Locate and identify every blood parasite.
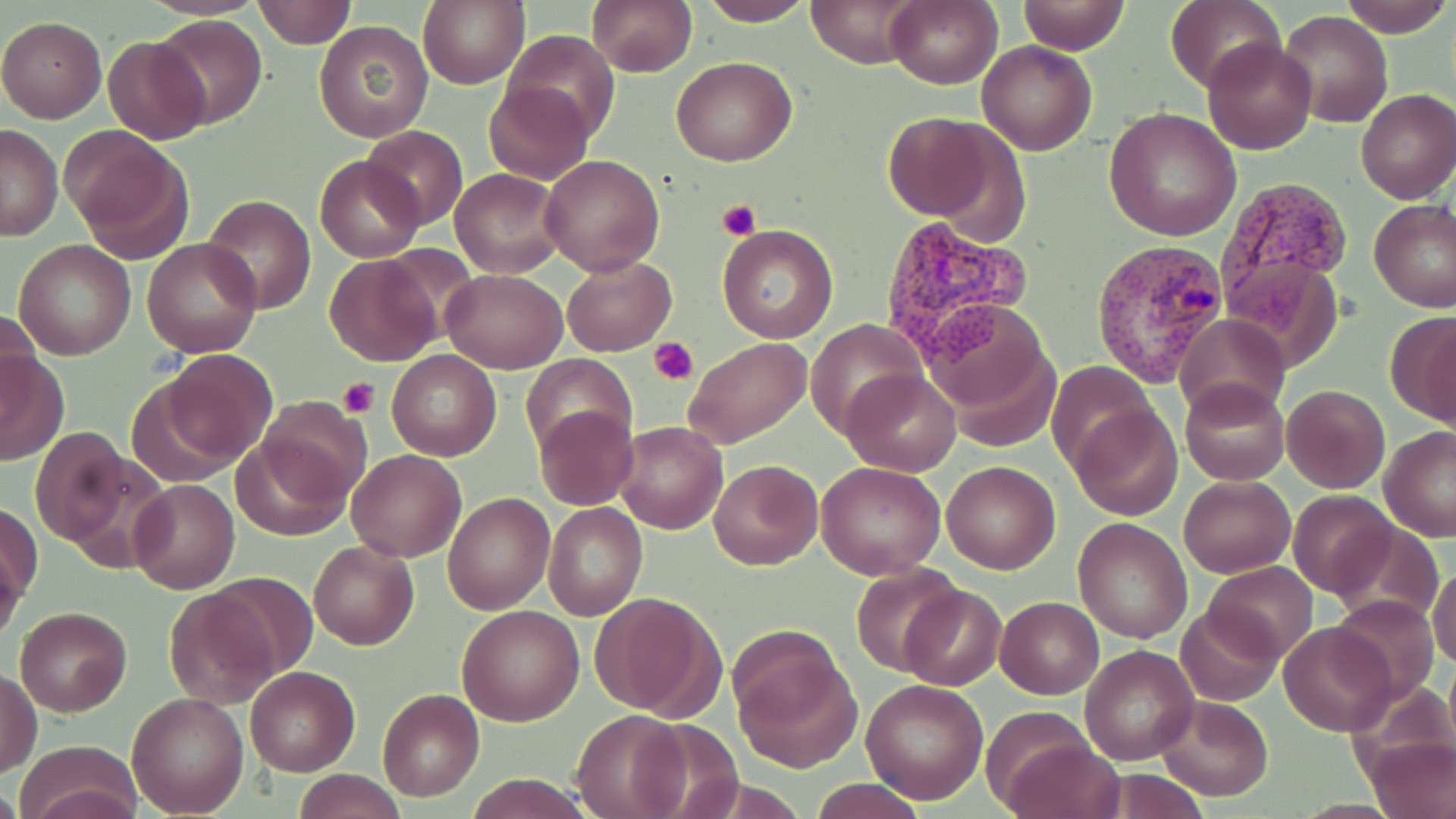

Approximate bounding boxes as (x1,y1)-(x2,y2) corner pairs in pixels.
Plasmodium vivax-infected red blood cells: (1218,177)-(1351,303), (875,213)-(1032,361), (1089,239)-(1229,387).
No Plasmodium falciparum, Plasmodium ovale, Plasmodium malariae, Babesia divergens, or Trypanosoma brucei observed.

slide_level_diagnosis: Plasmodium vivax
field_of_view: one of a larger specimen
platelet_locations: 'approximate bounding boxes as (x1,y1)-(x2,y2) corner pairs in pixels: (718,199)-(760,240), (649,338)-(697,384), (339,376)-(380,417)'
stain: May-Grünwald-Giemsa
magnification: 1000x
image_size: 1456×819 pixels
modality: optical microscopy
preparation: thin blood smear
uninfected_red_blood_cell_locations: 'approximate bounding boxes as (x1,y1)-(x2,y2) corner pairs in pixels: (251,0)-(354,47), (417,0)-(528,89), (587,0)-(697,76), (696,0)-(817,26), (808,0)-(919,68), (885,0)-(1002,89), (1015,0)-(1130,54), (1340,0)-(1454,37), (1165,2)-(1286,94), (1278,10)-(1393,127), (152,14)-(267,129), (0,16)-(106,122), (313,19)-(434,143), (503,30)-(618,138), (103,35)-(212,145), (1202,37)-(1318,155), (977,39)-(1097,156), (673,56)-(796,167), (483,80)-(593,185), (1355,90)-(1456,204), (1104,108)-(1242,243), (883,112)-(1004,221), (0,125)-(62,240), (360,125)-(467,233), (64,128)-(189,256), (315,154)-(423,262), (540,155)-(667,275), (450,168)-(565,278), (203,195)-(316,313), (1370,198)-(1456,311), (716,224)-(839,343), (13,239)-(137,360), (141,239)-(263,358), (325,254)-(441,365), (561,255)-(675,356), (1224,256)-(1344,369), (440,270)-(568,373), (415,280)-(548,430), (922,297)-(1052,419), (2,308)-(42,405), (1385,309)-(1456,428), (1175,314)-(1289,421), (806,320)-(929,435), (684,338)-(811,450), (0,348)-(68,464), (386,350)-(502,460), (154,352)-(276,469), (520,354)-(637,455), (1046,361)-(1155,470), (842,368)-(961,475), (1179,380)-(1289,484), (1283,384)-(1389,492), (254,397)-(372,507), (1069,403)-(1182,520), (535,405)-(638,512), (614,422)-(728,534), (1380,426)-(1456,541), (31,429)-(131,548), (231,432)-(352,541), (52,447)-(176,572), (346,449)-(466,561), (708,459)-(822,570), (942,461)-(1059,574), (817,462)-(947,581), (395,468)-(531,597), (1178,474)-(1296,577), (128,478)-(240,595), (443,491)-(556,615), (1289,491)-(1397,600), (1,501)-(41,611), (544,503)-(646,620), (1073,517)-(1193,643), (1327,521)-(1442,629), (308,539)-(419,650), (0,548)-(25,645), (1203,561)-(1318,663), (850,563)-(964,676), (1429,568)-(1456,670), (204,572)-(323,679), (898,585)-(1005,691), (164,588)-(279,708), (591,592)-(724,720), (1332,595)-(1439,702), (996,596)-(1104,698), (1174,604)-(1284,706), (457,605)-(585,726), (15,607)-(132,716), (1278,621)-(1397,736), (730,626)-(856,768), (1081,645)-(1198,764), (245,666)-(358,775), (1,669)-(42,777), (860,678)-(988,805), (377,688)-(484,801), (126,691)-(250,815), (1153,695)-(1273,803), (571,708)-(689,818), (997,735)-(1126,819), (1366,735)-(1454,819), (15,740)-(143,818), (292,770)-(407,819), (464,774)-(595,817), (807,778)-(927,819)'